State which parasite is depicted.
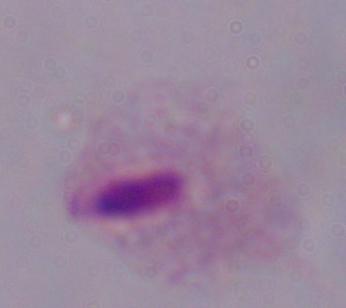
This is a trichomonad.

Photomicrograph. Captured at 1000x magnification.